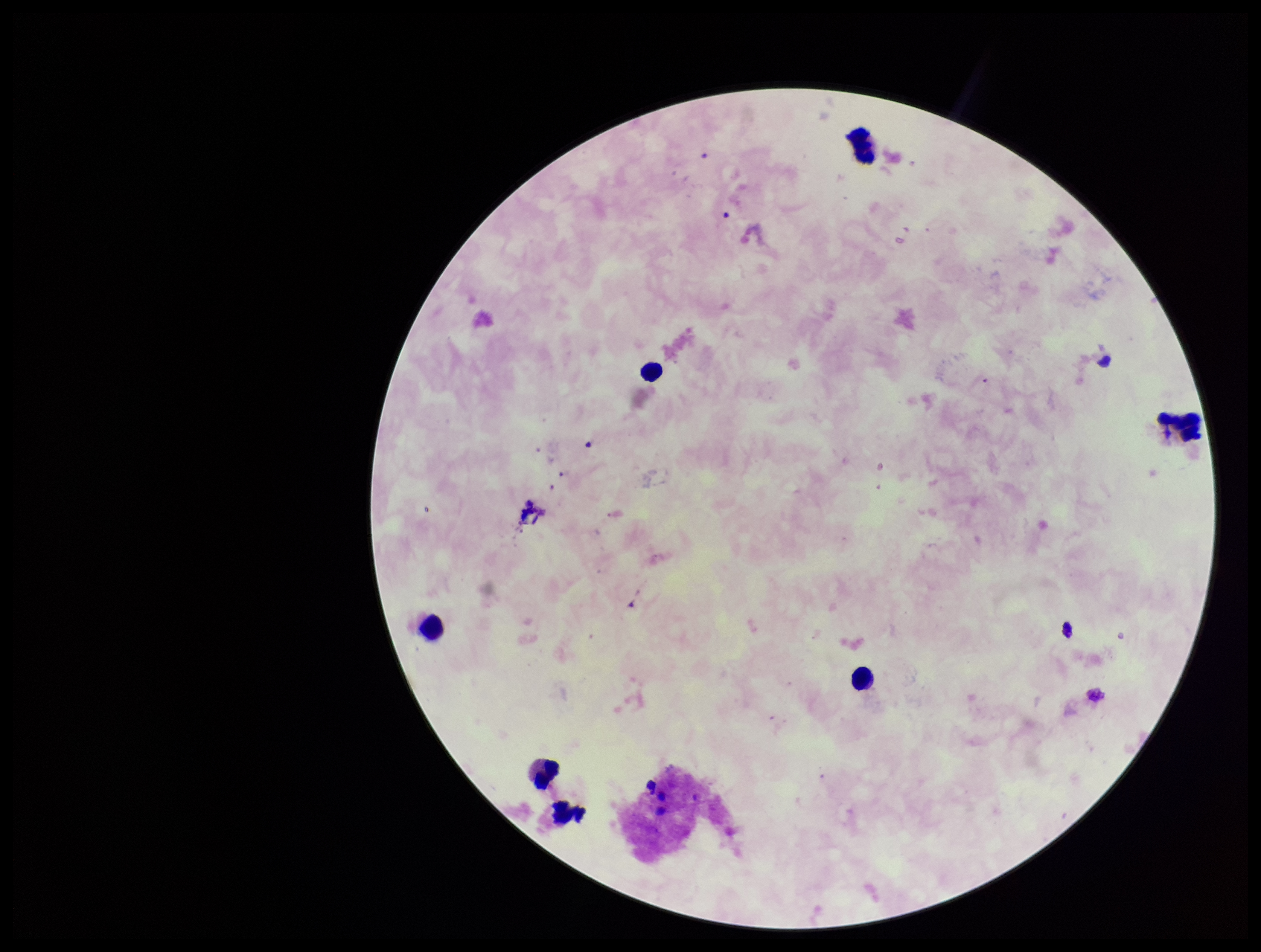 Giemsa stain. One field from this slide. Parasite count: 0. Image is 1261×952 pixels. Preparation: thick blood smear. Plasmodium parasites: none seen. Leukocyte count: 7. Patient malaria status: negative. Smartphone photograph taken through the eyepiece of a microscope.